Classify this cell by malaria status.
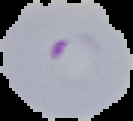

It is parasitized.

From a thin blood smear. The area outside the segmented cell region is set to black. Image is 133×121 pixels.